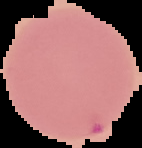
{
  "image_size": "142×148 pixels",
  "result": "Plasmodium parasites detected",
  "image_type": "segmented cell region on a black background",
  "preparation": "thin blood smear"
}